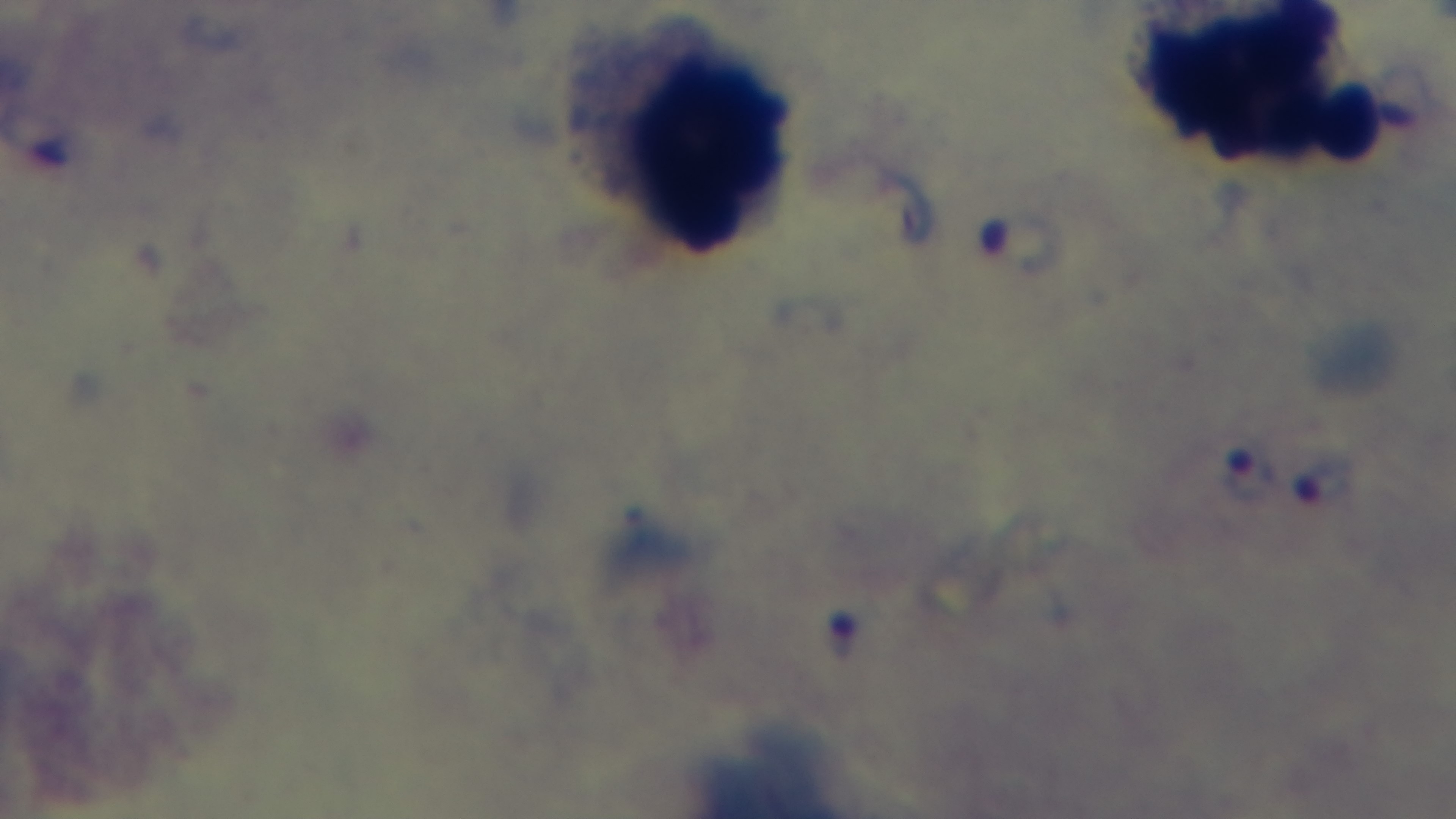 Light microscopy. Mounted 4K digital camera. 100x oil-immersion objective. Giemsa stain. Single field of view. Preparation: thick smear. Malaria status: positive.